Look for parasitized red blood cells.
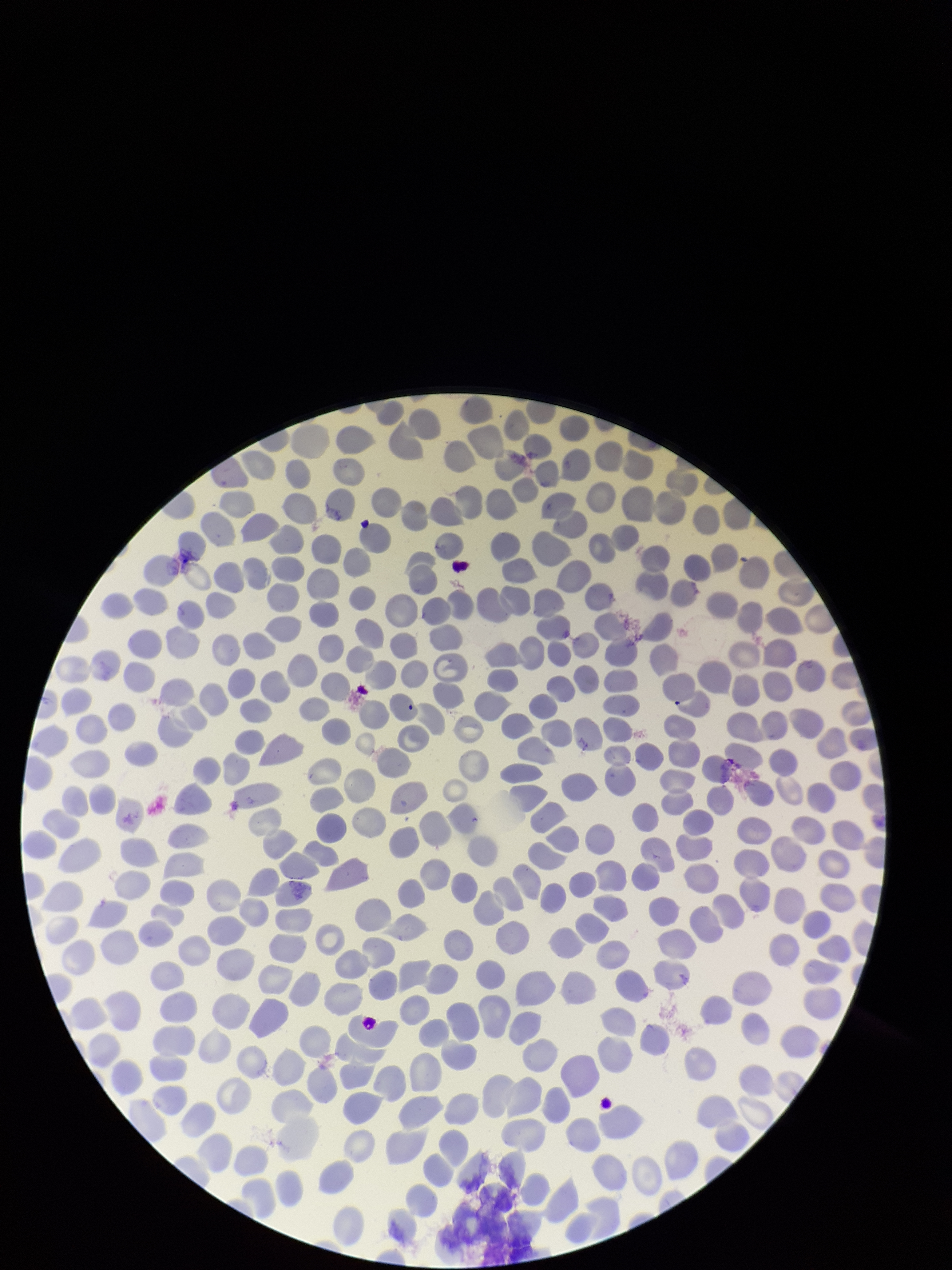
None identified.

Red blood cell count: 327. Preparation: thin smear. Single field of view. Image is 952×1270 pixels. Smartphone photograph taken through the eyepiece of a microscope. Parasitized red blood cell count: 0. Patient malaria status: negative. Stained with Giemsa.